Classify this cell by malaria status.
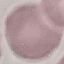

It is uninfected.

Summary:
  - Stain: Giemsa
  - Preparation: thin blood smear
  - Image type: cell patch, automatically extracted from a larger field of view and resized to 64 × 64 pixels
  - Capture: smartphone through the microscope eyepiece